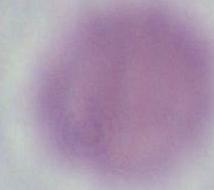

magnification: 1000x
identification: erythrocyte
modality: photomicrograph